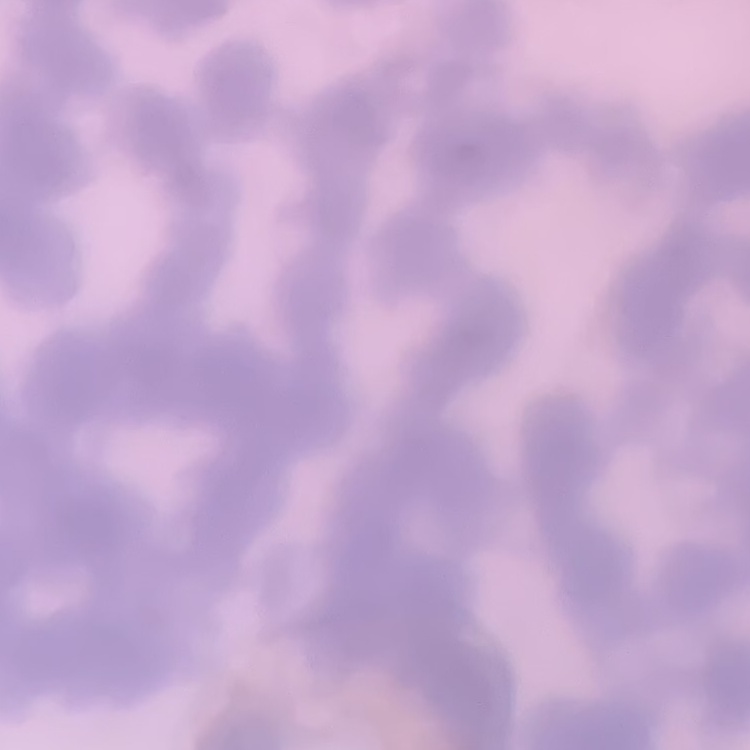
red blood cell morphology = rouleaux formation
stain = Field's or Giemsa
preparation = thin blood smear
image type = square crop of a larger photomicrograph